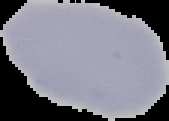

Malaria status: uninfected. Cell region segmented out of the field of view; the surrounding area is masked to black. Image is 169×121 pixels. From a thin blood smear.